Outline each uninfected red blood cell.
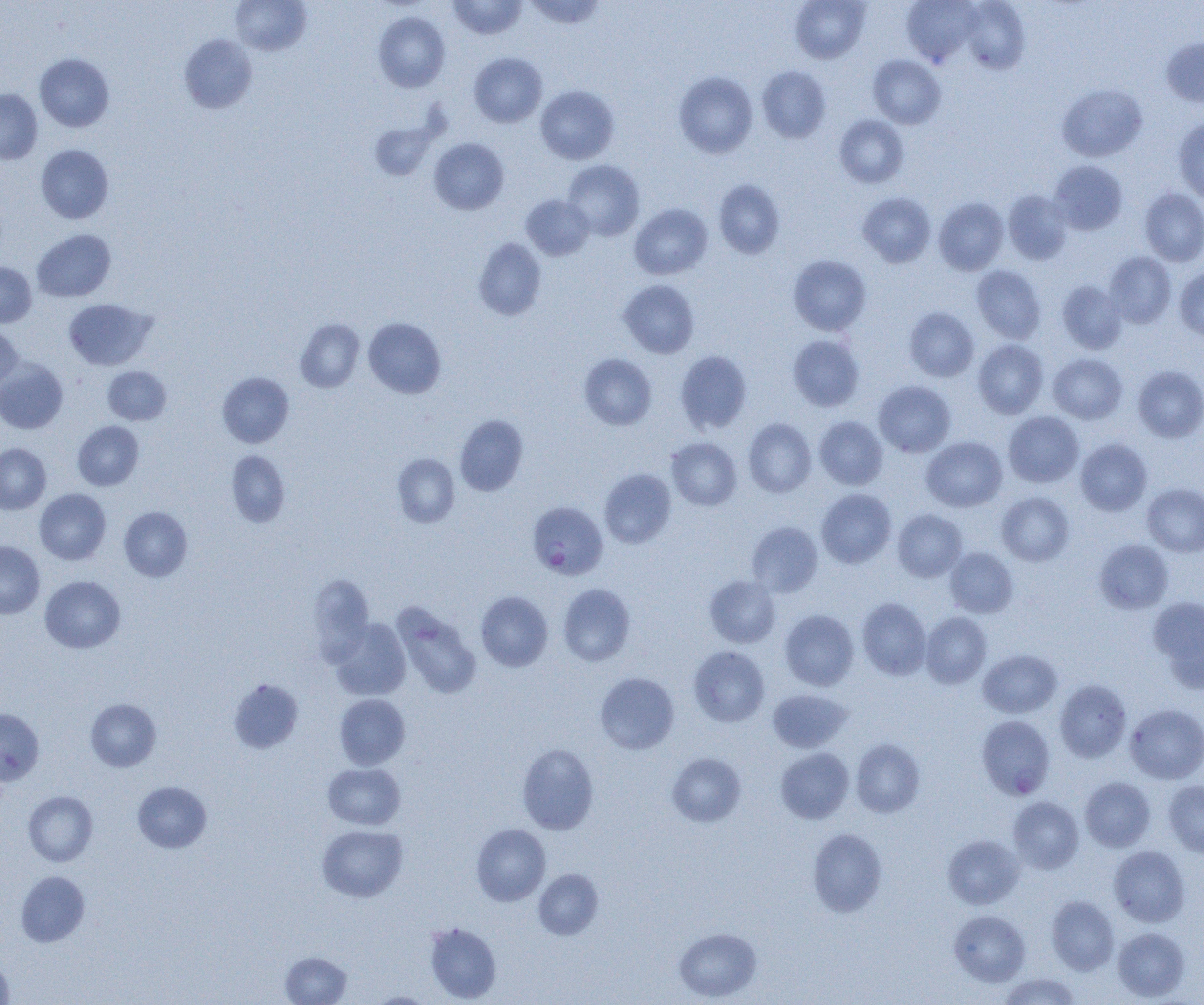

Approximate bounding boxes as (x1,y1)-(x2,y2) corner pairs in pixels.
Uninfected red blood cells: (447,0)-(527,39), (525,0)-(606,30), (790,0)-(871,63), (901,0)-(980,67), (231,1)-(312,56), (961,1)-(1029,74), (373,11)-(450,92), (179,33)-(257,114), (1161,37)-(1204,108), (469,52)-(547,127), (34,53)-(115,132), (868,55)-(945,128), (757,66)-(831,143), (674,71)-(758,158), (1057,83)-(1147,162), (535,85)-(619,164), (0,89)-(42,164), (834,115)-(909,188), (1173,115)-(1204,203), (369,120)-(437,180), (429,138)-(509,214), (36,144)-(114,224), (562,160)-(645,240), (1049,160)-(1127,234), (713,179)-(785,258), (1139,188)-(1204,266), (1003,190)-(1072,265), (858,192)-(936,267), (521,195)-(594,260), (933,197)-(1009,275), (629,203)-(713,280), (32,229)-(116,302), (473,238)-(546,321), (1104,251)-(1176,328), (788,254)-(872,335), (0,262)-(36,327), (971,265)-(1046,344), (1174,267)-(1204,340), (618,279)-(699,358), (1057,280)-(1127,354), (63,298)-(156,370), (904,306)-(979,381), (363,317)-(446,398), (295,318)-(365,393), (0,326)-(22,391), (788,334)-(865,411), (973,339)-(1048,418), (675,350)-(752,434), (579,353)-(657,430), (1048,353)-(1127,423), (0,358)-(68,434), (1133,365)-(1204,443), (103,366)-(171,425), (217,372)-(294,448), (874,380)-(955,457), (1003,411)-(1084,487), (454,414)-(528,495), (814,416)-(888,489), (743,418)-(816,497), (73,420)-(144,490), (922,436)-(1007,512), (666,437)-(742,511), (1075,438)-(1152,515), (0,443)-(51,515), (226,451)-(290,526), (392,453)-(460,528), (599,468)-(676,548), (1142,483)-(1204,556), (34,488)-(110,565), (816,488)-(896,568), (997,492)-(1074,566), (119,506)-(192,581), (892,509)-(966,581), (747,522)-(823,597), (1094,540)-(1173,614), (0,541)-(45,619), (945,547)-(1018,618), (307,574)-(374,663), (40,575)-(125,653), (704,575)-(781,648), (558,583)-(636,666), (475,591)-(553,671), (1148,596)-(1204,686), (857,597)-(931,680), (392,602)-(482,699), (779,609)-(859,690), (921,612)-(992,688), (329,618)-(411,700), (688,646)-(770,726), (978,649)-(1062,718), (595,672)-(679,754), (229,679)-(303,754), (1054,679)-(1132,762), (768,688)-(851,752), (334,694)-(410,770), (85,698)-(161,771), (1125,703)-(1204,783), (0,708)-(44,785), (977,715)-(1055,800), (851,738)-(925,818), (517,744)-(599,834), (775,747)-(854,823), (667,753)-(746,827), (323,763)-(405,830), (1079,776)-(1155,851), (1163,780)-(1204,857), (132,781)-(212,852), (23,791)-(97,866), (1008,796)-(1084,873), (471,824)-(551,905), (317,825)-(408,902), (807,828)-(887,917), (943,834)-(1024,909), (1108,845)-(1190,927), (533,868)-(604,940), (16,871)-(89,946), (1046,895)-(1119,975), (949,910)-(1031,986), (424,922)-(501,1003), (674,927)-(762,1002), (1113,927)-(1190,1001), (280,951)-(352,1005), (0,955)-(14,1003), (998,973)-(1081,1004), (367,992)-(436,1005).

Plasmodium falciparum-infected red blood cell locations: (528,501)-(608,579). Slide-level diagnosis: Plasmodium falciparum. Light microscopy. 1000x magnification. Thin blood smear. Single field of view. Image is 1204×1005 pixels.